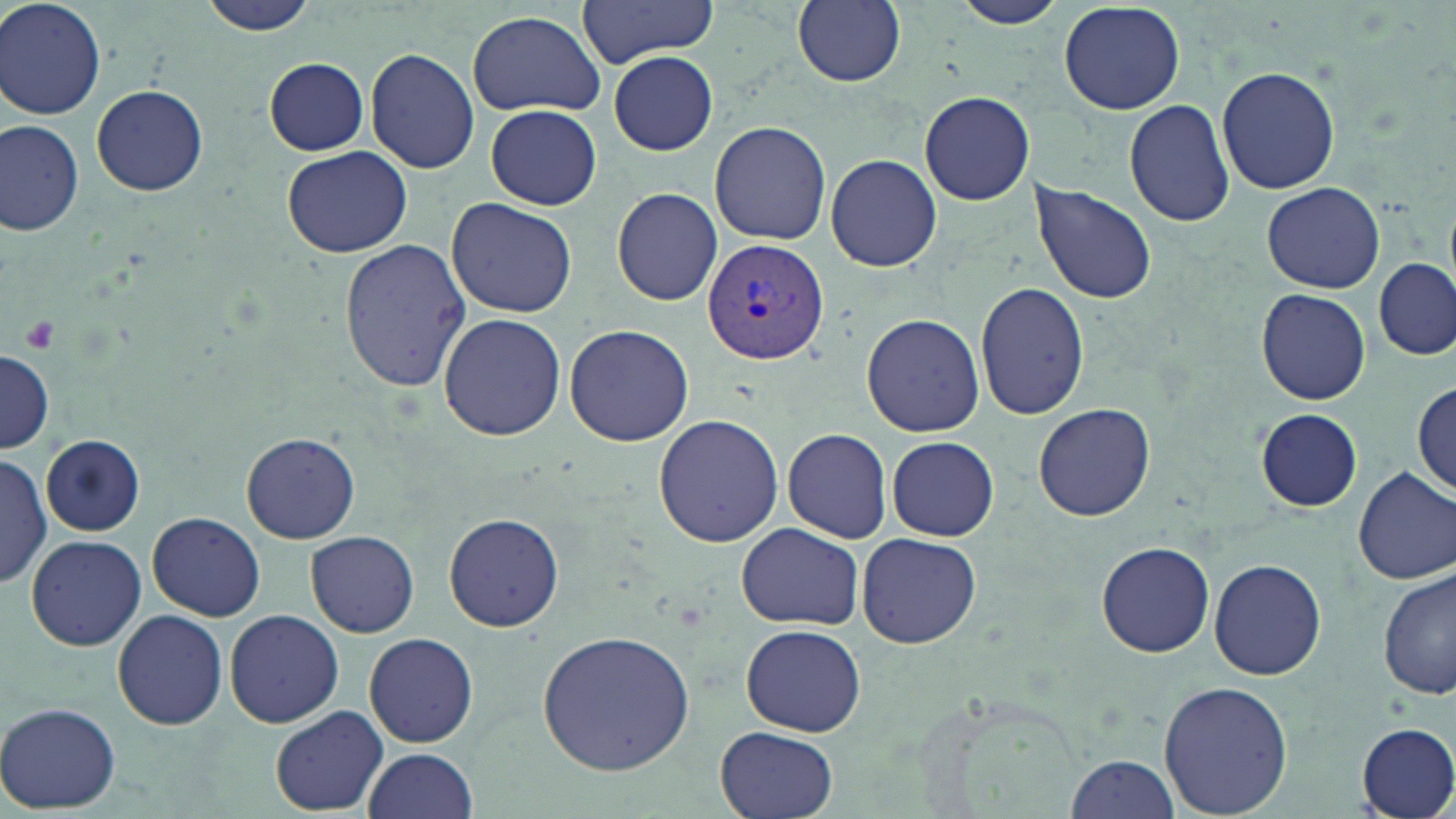

Summary:
  - Coordinate format: approximate bounding boxes as named x1/y1/x2/y2 corners in pixels
  - Uninfected red blood cell locations: (x1=0, y1=0, x2=106, y2=119), (x1=197, y1=0, x2=324, y2=38), (x1=574, y1=0, x2=723, y2=67), (x1=792, y1=0, x2=906, y2=88), (x1=947, y1=1, x2=1070, y2=30), (x1=1058, y1=2, x2=1187, y2=115), (x1=465, y1=11, x2=608, y2=119), (x1=366, y1=48, x2=481, y2=175), (x1=608, y1=51, x2=718, y2=155), (x1=263, y1=57, x2=370, y2=155), (x1=1216, y1=65, x2=1341, y2=194), (x1=92, y1=84, x2=208, y2=197), (x1=918, y1=91, x2=1034, y2=206), (x1=1124, y1=98, x2=1234, y2=227), (x1=481, y1=104, x2=604, y2=209), (x1=1, y1=119, x2=85, y2=236), (x1=708, y1=121, x2=832, y2=245), (x1=282, y1=144, x2=412, y2=258), (x1=826, y1=154, x2=942, y2=272), (x1=1030, y1=181, x2=1159, y2=307), (x1=1261, y1=182, x2=1385, y2=292), (x1=611, y1=187, x2=723, y2=307), (x1=446, y1=197, x2=578, y2=319), (x1=339, y1=239, x2=471, y2=392), (x1=1374, y1=257, x2=1454, y2=360), (x1=975, y1=281, x2=1090, y2=420), (x1=1255, y1=288, x2=1372, y2=406), (x1=438, y1=312, x2=565, y2=442), (x1=860, y1=313, x2=984, y2=436), (x1=563, y1=323, x2=693, y2=447), (x1=1, y1=350, x2=52, y2=452), (x1=1414, y1=377, x2=1455, y2=498), (x1=1033, y1=401, x2=1156, y2=522), (x1=1255, y1=408, x2=1363, y2=512), (x1=653, y1=414, x2=784, y2=546), (x1=783, y1=431, x2=892, y2=543), (x1=240, y1=432, x2=361, y2=545), (x1=41, y1=436, x2=144, y2=535), (x1=887, y1=436, x2=999, y2=541), (x1=0, y1=451, x2=49, y2=592), (x1=1353, y1=466, x2=1456, y2=586), (x1=148, y1=510, x2=266, y2=622), (x1=443, y1=512, x2=565, y2=632), (x1=736, y1=522, x2=864, y2=632), (x1=305, y1=530, x2=418, y2=638), (x1=855, y1=533, x2=982, y2=648), (x1=26, y1=534, x2=147, y2=650), (x1=1096, y1=540, x2=1216, y2=658), (x1=1209, y1=559, x2=1326, y2=681), (x1=1377, y1=567, x2=1454, y2=703), (x1=113, y1=609, x2=229, y2=730), (x1=225, y1=609, x2=343, y2=729), (x1=740, y1=623, x2=867, y2=737), (x1=537, y1=629, x2=696, y2=777), (x1=364, y1=632, x2=479, y2=748), (x1=1159, y1=680, x2=1292, y2=817), (x1=1, y1=702, x2=122, y2=813), (x1=271, y1=705, x2=387, y2=816), (x1=1356, y1=723, x2=1456, y2=818), (x1=713, y1=724, x2=840, y2=819), (x1=362, y1=747, x2=480, y2=819), (x1=1065, y1=754, x2=1181, y2=818)
  - Platelet locations: (x1=22, y1=316, x2=58, y2=352)
  - Plasmodium vivax-infected red blood cell locations: (x1=702, y1=239, x2=831, y2=364)
  - Slide-level diagnosis: Plasmodium vivax
  - Preparation: thin blood film
  - Magnification: 1000x
  - Modality: optical microscopy
  - Field of view: single
  - Stain: May-Grünwald-Giemsa
  - Image size: 1456×819 pixels